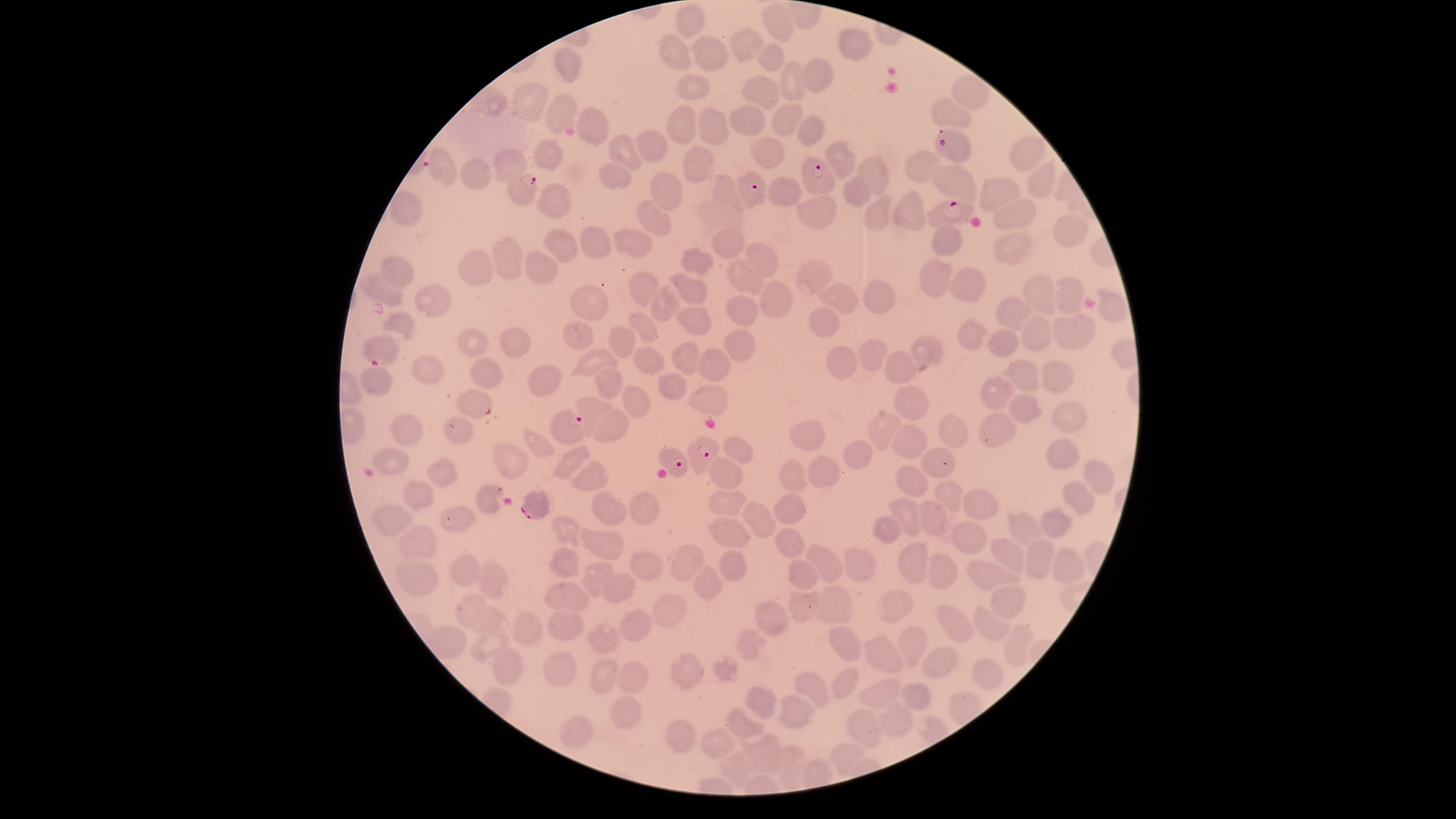 Approximate marker points, in pixels from the top-left corner. Parasitized red blood cells: (x=953, y=143), (x=821, y=178), (x=521, y=188), (x=749, y=188), (x=942, y=212), (x=378, y=347), (x=567, y=427), (x=704, y=451), (x=674, y=459), (x=535, y=504). Uninfected red blood cells: (x=688, y=13), (x=778, y=21), (x=855, y=43), (x=745, y=45), (x=670, y=50), (x=708, y=53), (x=772, y=57), (x=571, y=65), (x=794, y=78), (x=817, y=78), (x=694, y=81), (x=758, y=88), (x=965, y=93), (x=492, y=99), (x=526, y=99), (x=947, y=110), (x=559, y=112), (x=787, y=117), (x=593, y=118), (x=746, y=119), (x=708, y=121), (x=682, y=124), (x=812, y=128), (x=652, y=145), (x=622, y=148), (x=550, y=151), (x=767, y=151), (x=1027, y=153), (x=838, y=156), (x=699, y=164), (x=920, y=164), (x=512, y=166), (x=442, y=168), (x=868, y=173), (x=608, y=174), (x=479, y=176), (x=958, y=176), (x=1032, y=177), (x=665, y=191), (x=722, y=191), (x=855, y=191), (x=996, y=192), (x=787, y=198), (x=556, y=200), (x=401, y=203), (x=879, y=207), (x=908, y=208), (x=714, y=211), (x=824, y=212), (x=1010, y=213), (x=658, y=222), (x=1064, y=237), (x=949, y=240), (x=734, y=241), (x=562, y=242), (x=602, y=242), (x=631, y=243), (x=1012, y=251), (x=757, y=255), (x=508, y=256), (x=704, y=261), (x=478, y=268), (x=544, y=270), (x=814, y=270), (x=750, y=271), (x=398, y=276), (x=936, y=278), (x=965, y=282), (x=640, y=285), (x=383, y=288), (x=874, y=290), (x=686, y=292), (x=1038, y=293), (x=843, y=296), (x=1066, y=296), (x=769, y=299), (x=433, y=300), (x=665, y=305), (x=593, y=306), (x=1012, y=307), (x=739, y=308), (x=1114, y=311), (x=824, y=319), (x=694, y=320), (x=403, y=321), (x=643, y=326), (x=1072, y=330), (x=578, y=333), (x=970, y=333), (x=622, y=335), (x=1042, y=336), (x=473, y=340), (x=996, y=343), (x=516, y=344), (x=737, y=344), (x=928, y=344), (x=875, y=350), (x=647, y=356), (x=686, y=357), (x=900, y=360), (x=595, y=361), (x=845, y=361), (x=712, y=366), (x=429, y=368), (x=491, y=374), (x=377, y=376), (x=1022, y=376), (x=1058, y=377), (x=547, y=378), (x=672, y=383), (x=608, y=385), (x=996, y=391), (x=470, y=396), (x=706, y=398), (x=633, y=399), (x=914, y=404), (x=600, y=407), (x=1027, y=412), (x=1072, y=417), (x=616, y=423), (x=998, y=423), (x=887, y=425), (x=414, y=430), (x=951, y=430), (x=807, y=431), (x=461, y=433), (x=906, y=437), (x=538, y=441), (x=742, y=448), (x=931, y=452), (x=1063, y=452), (x=857, y=454), (x=388, y=455), (x=504, y=457), (x=571, y=461), (x=444, y=470), (x=719, y=470), (x=820, y=470), (x=792, y=472), (x=591, y=473), (x=916, y=478), (x=1097, y=478), (x=415, y=483), (x=944, y=495), (x=1083, y=495), (x=487, y=497), (x=725, y=500), (x=791, y=501), (x=980, y=502), (x=611, y=509), (x=652, y=510), (x=909, y=513), (x=395, y=519), (x=758, y=519), (x=932, y=519), (x=1053, y=523), (x=1024, y=525), (x=573, y=527), (x=724, y=530), (x=885, y=531), (x=967, y=539), (x=607, y=540), (x=788, y=540), (x=424, y=541), (x=1004, y=551), (x=565, y=557), (x=823, y=558), (x=1042, y=558), (x=691, y=561), (x=916, y=561), (x=859, y=562), (x=648, y=564), (x=1063, y=564), (x=461, y=566), (x=734, y=566), (x=949, y=569), (x=803, y=574), (x=988, y=574), (x=596, y=575), (x=418, y=580), (x=707, y=583), (x=494, y=584), (x=619, y=588), (x=1005, y=596), (x=564, y=598), (x=834, y=601), (x=900, y=602), (x=804, y=603), (x=471, y=606), (x=672, y=609), (x=771, y=619), (x=491, y=621), (x=570, y=623), (x=634, y=623), (x=989, y=624), (x=522, y=625), (x=955, y=627), (x=607, y=636), (x=850, y=639), (x=749, y=640), (x=908, y=642), (x=490, y=643), (x=1013, y=646), (x=882, y=654), (x=943, y=663), (x=724, y=666), (x=505, y=667), (x=565, y=667), (x=689, y=668), (x=992, y=671), (x=602, y=672), (x=629, y=674), (x=847, y=682), (x=811, y=683), (x=881, y=692), (x=916, y=692), (x=764, y=700), (x=627, y=706), (x=794, y=709), (x=747, y=724), (x=896, y=725), (x=866, y=726), (x=574, y=731), (x=678, y=733), (x=721, y=742), (x=768, y=752), (x=847, y=753), (x=791, y=761), (x=740, y=766). Smartphone photograph through the microscope eyepiece. Giemsa stain. Thin blood smear. Species: Plasmodium falciparum. Circular visible region. Image is 1456×819 pixels. Presence: malaria parasites detected. One field of view of the specimen.